Classify this cell by malaria status.
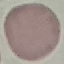

It is uninfected.

Thin smear of blood. Giemsa stain. Photographed with a smartphone camera at the microscope eyepiece. Automatically extracted cell patch, resized to 64 × 64 pixels.